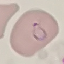

Malaria status: parasitized. Acquired by smartphone through the microscope eyepiece. Thin blood film. Cell patch, automatically extracted from a larger field of view and resized to 64 × 64 pixels. Giemsa-stained preparation.